Classify this cell by malaria status.
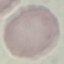

It is uninfected.

Cell patch, automatically extracted from a larger field of view and resized to 64 × 64 pixels. Acquired by smartphone through the microscope eyepiece. Giemsa-stained preparation. Thin blood smear.